Assess this cell for malaria.
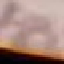
It is uninfected.

Summary:
  - Image type: automatically extracted cell patch, resized to 64 × 64 pixels
  - Capture: smartphone camera at the microscope eyepiece
  - Preparation: thin blood film
  - Stain: Giemsa